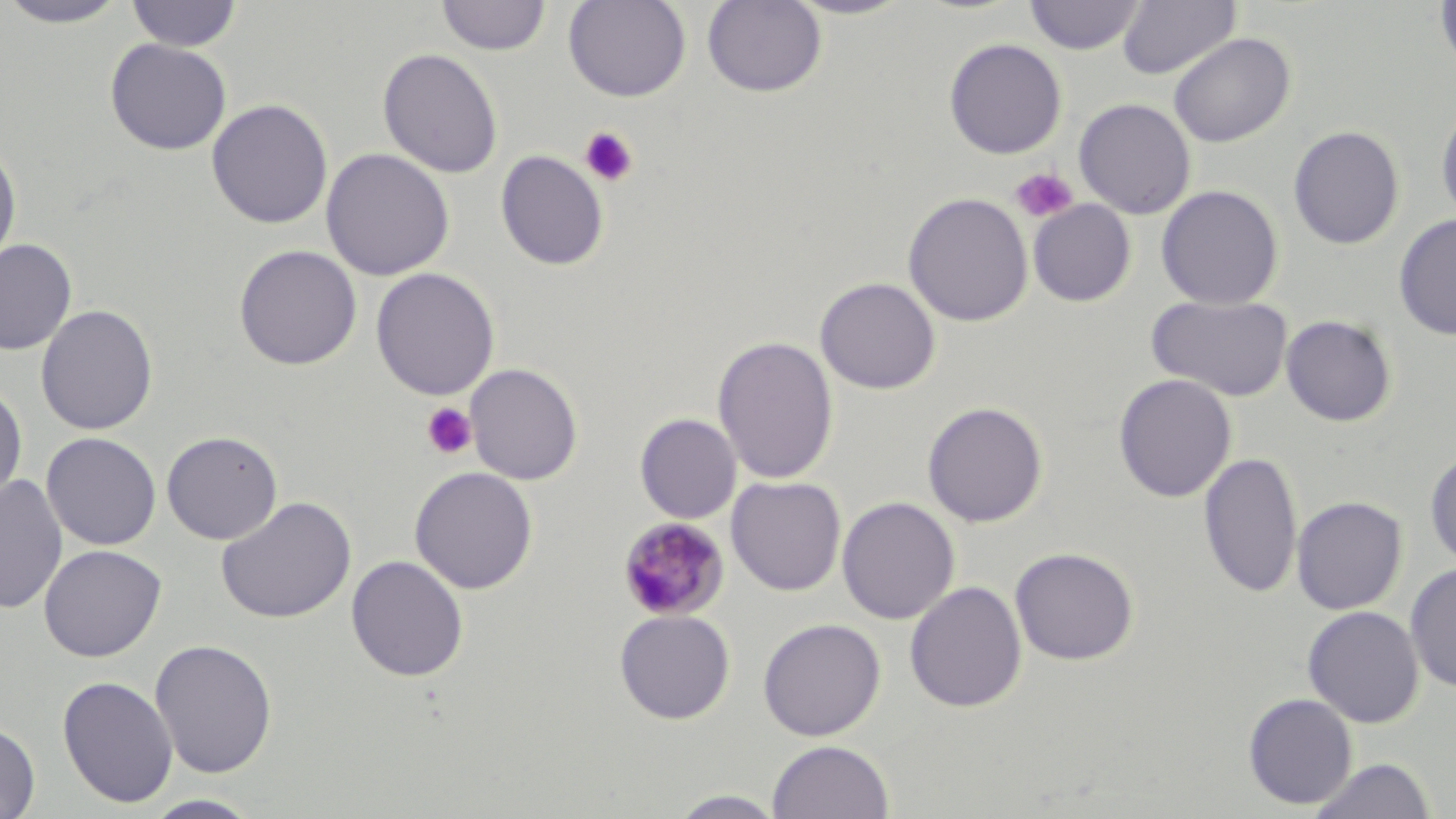

Approximate bounding boxes as (x1,y1)-(x2,y2) corner pairs in pixels. Platelet locations: (579,125)-(639,187), (1010,167)-(1079,224), (421,403)-(478,460). Plasmodium malariae-infected red blood cell locations: (616,517)-(731,622). Uninfected red blood cell locations: (126,0)-(243,52), (437,0)-(550,56), (563,0)-(691,102), (702,0)-(827,97), (785,0)-(916,20), (1024,0)-(1146,55), (1117,0)-(1240,80), (1435,0)-(1456,73), (0,1)-(131,28), (1168,32)-(1296,148), (105,38)-(232,155), (944,38)-(1066,159), (377,48)-(503,178), (206,98)-(333,230), (1073,98)-(1196,219), (1436,99)-(1456,226), (1288,125)-(1404,250), (0,138)-(22,272), (320,148)-(454,281), (496,150)-(609,271), (1156,185)-(1283,309), (902,192)-(1033,327), (1027,199)-(1136,307), (1393,214)-(1456,341), (0,238)-(77,356), (234,244)-(362,370), (370,268)-(500,400), (815,277)-(941,395), (1146,294)-(1293,402), (36,304)-(158,435), (1281,315)-(1397,427), (713,336)-(838,484), (464,363)-(583,485), (1113,374)-(1237,502), (0,382)-(27,507), (922,401)-(1048,528), (635,414)-(742,524), (161,430)-(283,545), (41,432)-(161,551), (1425,450)-(1456,569), (1198,451)-(1302,598), (409,466)-(538,595), (0,473)-(67,615), (727,476)-(846,595), (216,496)-(357,624), (836,496)-(960,624), (1291,496)-(1407,615), (39,544)-(166,661), (1010,547)-(1139,666), (346,555)-(469,682), (1405,564)-(1456,692), (904,580)-(1027,713), (1302,605)-(1424,728), (614,608)-(735,724), (758,618)-(886,741), (149,638)-(278,778), (57,675)-(178,808), (1243,692)-(1359,809), (0,721)-(40,818), (767,739)-(894,819), (1310,758)-(1436,818), (666,790)-(789,818), (142,794)-(264,818). Slide-level diagnosis: Plasmodium malariae. Thin blood film. Image is 1456×819 pixels. Single field of view. Light microscopy. 1000x magnification. May-Grünwald-Giemsa stain.